State the blood parasite species.
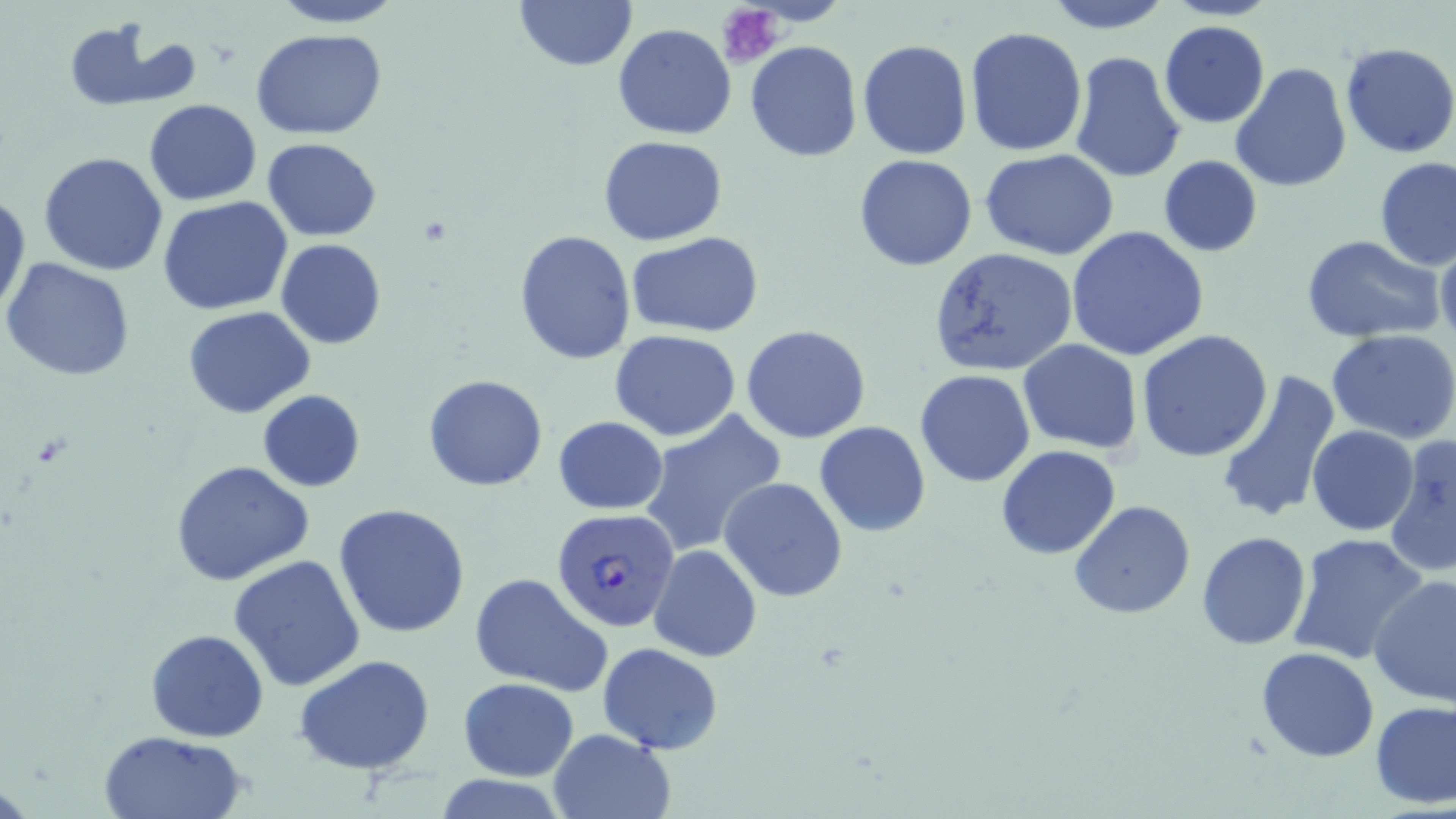
Plasmodium falciparum.

Approximate bounding boxes as [x1, y1, x2, y2] in pixels. Platelet locations: [717, 4, 784, 69]. Plasmodium falciparum-infected red blood cell locations: [551, 507, 680, 635]. Uninfected red blood cell locations: [264, 0, 410, 28], [514, 0, 638, 73], [1040, 0, 1174, 33], [62, 18, 191, 108], [1159, 20, 1271, 128], [612, 23, 736, 139], [965, 27, 1086, 157], [250, 30, 389, 140], [857, 39, 973, 160], [745, 40, 862, 161], [1340, 42, 1456, 159], [1069, 50, 1185, 183], [1230, 61, 1352, 194], [143, 100, 262, 206], [598, 135, 728, 244], [263, 137, 381, 239], [980, 149, 1120, 259], [38, 152, 170, 276], [854, 155, 977, 271], [1157, 156, 1263, 258], [1375, 157, 1456, 271], [0, 190, 30, 318], [157, 195, 294, 315], [1065, 225, 1210, 361], [515, 229, 636, 364], [628, 232, 765, 338], [1302, 235, 1444, 341], [276, 239, 387, 348], [1435, 239, 1456, 344], [928, 247, 1080, 378], [2, 257, 134, 383], [183, 306, 316, 418], [740, 324, 872, 444], [1328, 329, 1456, 443], [610, 330, 741, 440], [1137, 330, 1274, 463], [1018, 339, 1143, 455], [915, 370, 1036, 487], [1213, 371, 1341, 525], [423, 375, 549, 490], [257, 390, 366, 492], [639, 409, 787, 558], [552, 417, 670, 514], [814, 420, 931, 537], [1306, 427, 1420, 535], [1385, 435, 1455, 578], [995, 445, 1121, 560], [171, 461, 316, 587], [720, 477, 848, 602], [1069, 499, 1197, 620], [333, 502, 472, 638], [1196, 532, 1311, 649], [1286, 533, 1430, 664], [649, 545, 761, 662], [227, 553, 367, 692], [469, 572, 612, 698], [1369, 573, 1456, 705], [145, 628, 269, 742], [596, 640, 724, 753], [1257, 647, 1380, 762], [294, 654, 437, 776], [458, 675, 581, 782], [1369, 699, 1456, 808], [97, 729, 247, 819], [546, 729, 676, 819]. One field of a larger specimen. Thin blood smear. Image is 1456×819 pixels. May-Grünwald-Giemsa stain. Optical microscopy. 1000x magnification.